Name the blood parasite species.
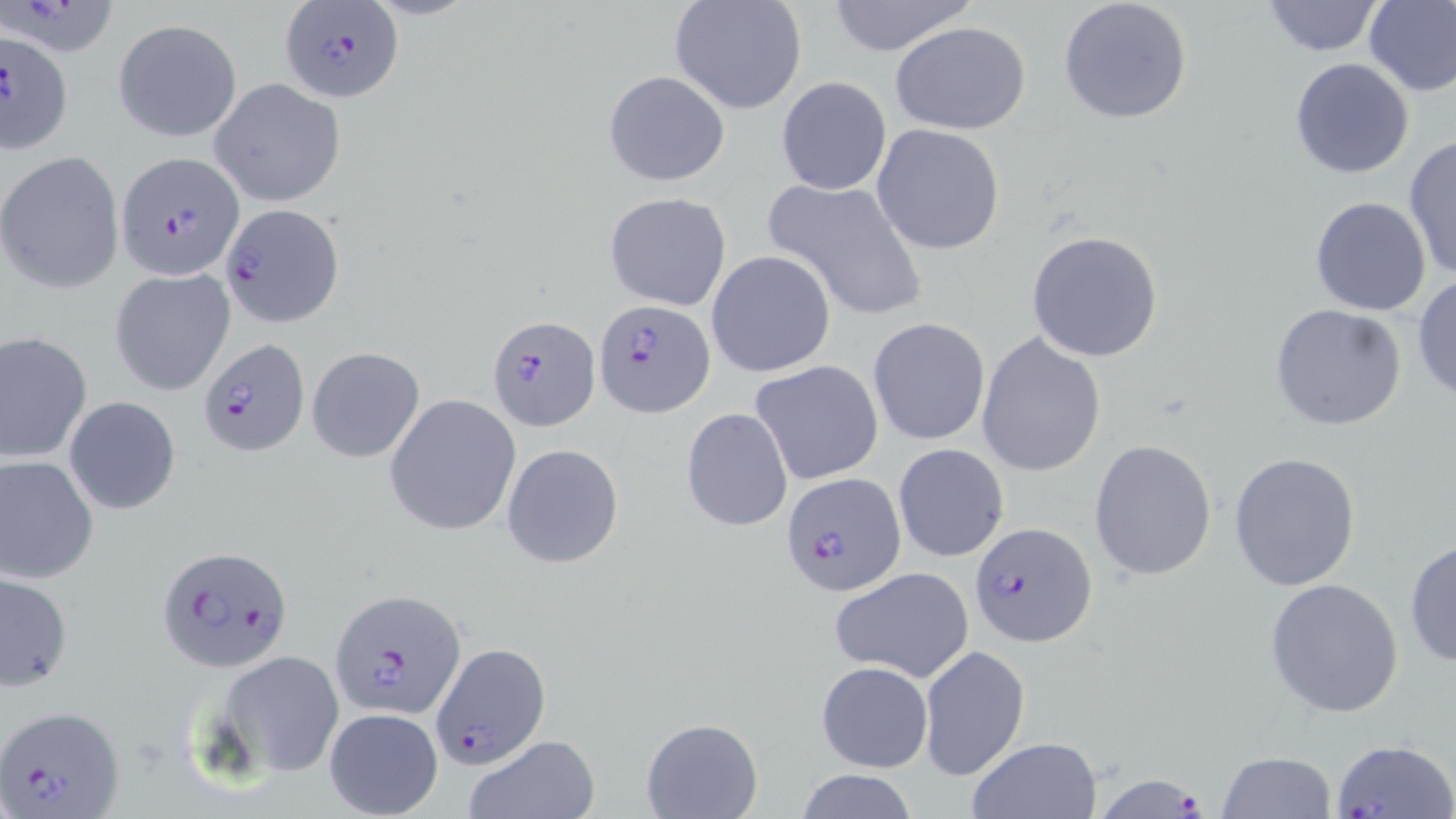
Plasmodium falciparum.

preparation = thin blood film
modality = light microscopy
field of view = one of a larger specimen
uninfected red blood cell locations = approximate bounding boxes as (x1, y1, x2, y2) in pixels: (668, 0, 807, 116), (823, 0, 977, 57), (1058, 0, 1193, 125), (1260, 0, 1385, 58), (1363, 1, 1456, 96), (112, 18, 243, 142), (889, 20, 1032, 135), (1288, 56, 1416, 180), (602, 69, 730, 187), (776, 76, 891, 196), (210, 78, 348, 207), (872, 123, 1005, 254), (1404, 135, 1456, 281), (1, 151, 125, 293), (762, 175, 928, 323), (603, 191, 731, 311), (1309, 195, 1432, 316), (1025, 229, 1165, 363), (706, 250, 836, 378), (109, 268, 236, 396), (1411, 273, 1456, 402), (1269, 303, 1407, 431), (867, 317, 991, 446), (0, 331, 94, 463), (977, 332, 1107, 478), (306, 346, 426, 463), (751, 361, 882, 486), (63, 395, 182, 516), (384, 395, 520, 537), (681, 407, 793, 532), (1088, 438, 1218, 582), (893, 443, 1009, 562), (501, 444, 625, 569), (1228, 452, 1362, 591), (0, 455, 99, 582), (1405, 537, 1456, 671), (829, 566, 975, 683), (0, 572, 72, 691), (1264, 579, 1405, 719), (919, 644, 1029, 780), (213, 649, 345, 779), (815, 660, 934, 773), (322, 706, 444, 818), (641, 717, 762, 819), (464, 736, 600, 819), (967, 737, 1103, 819), (1216, 751, 1337, 818), (790, 770, 924, 818)
magnification = 1000x
stain = May-Grünwald-Giemsa
Plasmodium falciparum-infected red blood cell locations = approximate bounding boxes as (x1, y1, x2, y2) in pixels: (0, 2, 122, 51), (282, 2, 400, 102), (0, 26, 76, 154), (115, 151, 246, 282), (220, 204, 346, 329), (592, 298, 716, 419), (486, 315, 601, 432), (198, 340, 312, 455), (781, 472, 907, 599), (968, 521, 1097, 649), (154, 543, 293, 673), (327, 588, 467, 719), (432, 642, 552, 770), (1, 704, 126, 818), (1331, 737, 1454, 818), (1097, 770, 1211, 819)
image size = 1456×819 pixels